Mark where platelets are.
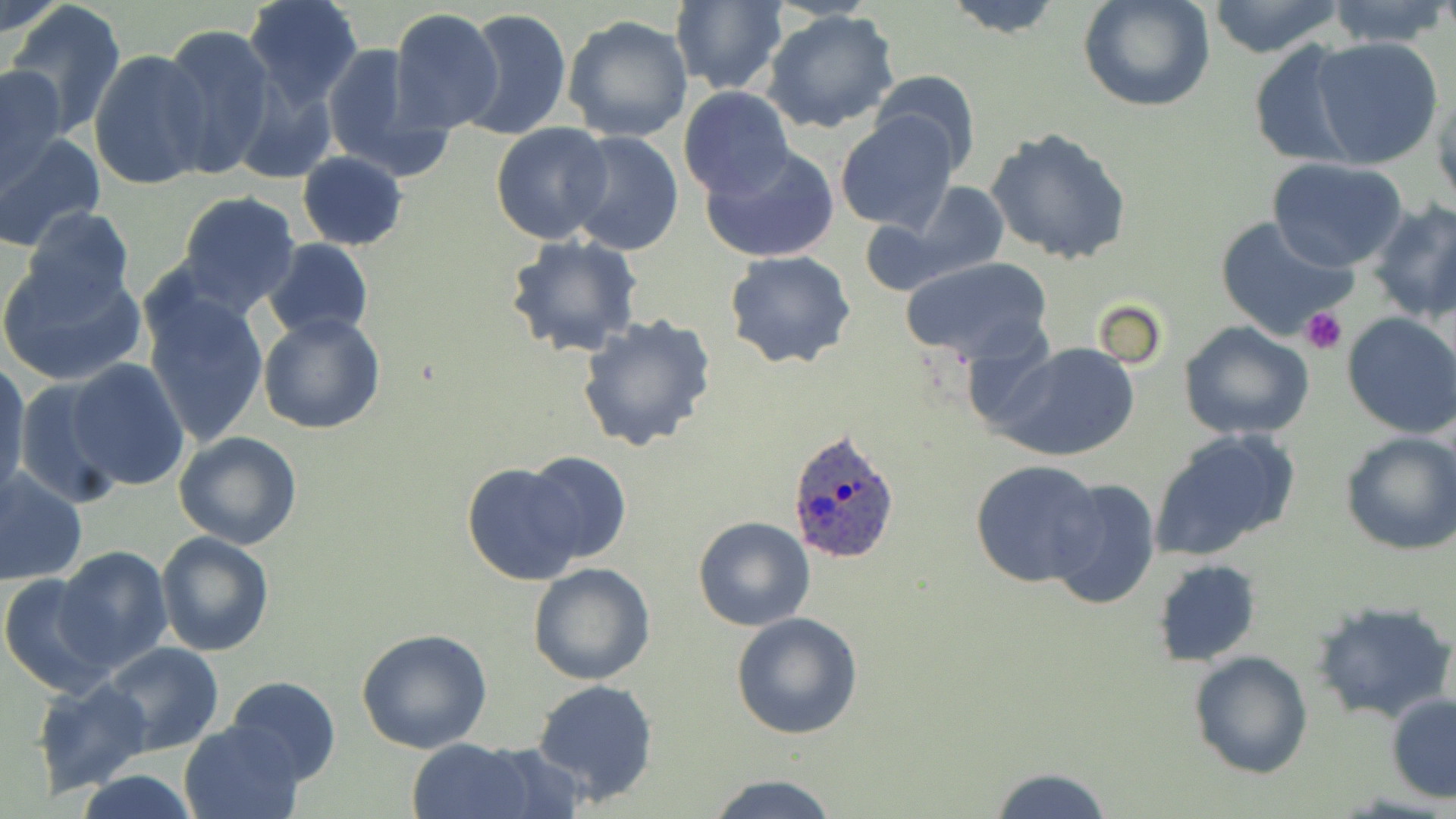

Approximate bounding boxes as [x1, y1, x2, y2] in pixels.
Platelets: [1299, 308, 1347, 355].

slide_level_diagnosis: Plasmodium ovale
preparation: thin blood film
uninfected_red_blood_cell_locations: 'approximate bounding boxes as [x1, y1, x2, y2] in pixels: [241, 0, 364, 106], [669, 0, 788, 96], [936, 0, 1068, 38], [1077, 0, 1216, 114], [1205, 0, 1346, 57], [1323, 0, 1455, 48], [1, 1, 68, 40], [5, 1, 128, 139], [389, 6, 503, 134], [457, 8, 573, 142], [763, 10, 901, 134], [562, 12, 693, 142], [158, 25, 280, 178], [1308, 37, 1444, 169], [320, 41, 450, 183], [1246, 43, 1365, 167], [87, 50, 214, 192], [2, 66, 70, 193], [869, 69, 981, 173], [228, 74, 338, 184], [677, 87, 796, 199], [835, 114, 958, 234], [491, 123, 616, 245], [983, 125, 1135, 267], [0, 128, 103, 250], [565, 131, 685, 256], [702, 144, 840, 264], [297, 151, 406, 250], [1267, 157, 1407, 272], [892, 181, 1012, 286], [177, 192, 303, 316], [1369, 200, 1456, 322], [20, 206, 136, 314], [1214, 216, 1358, 341], [504, 234, 644, 360], [263, 238, 375, 340], [724, 251, 858, 370], [900, 256, 1056, 368], [0, 258, 148, 387], [141, 288, 269, 448], [1343, 311, 1456, 438], [258, 312, 386, 434], [574, 312, 717, 453], [1178, 321, 1314, 440], [995, 343, 1143, 461], [67, 358, 191, 491], [1, 361, 30, 495], [10, 377, 125, 507], [1148, 428, 1301, 561], [174, 431, 303, 550], [1339, 431, 1456, 556], [521, 450, 632, 567], [971, 458, 1106, 588], [462, 462, 588, 585], [0, 467, 86, 587], [1045, 476, 1161, 611], [693, 516, 815, 631], [154, 530, 275, 657], [56, 546, 173, 672], [1152, 559, 1262, 667], [528, 562, 656, 685], [0, 573, 117, 698], [1309, 598, 1455, 725], [730, 611, 863, 740], [356, 629, 495, 754], [100, 640, 224, 757], [1188, 650, 1314, 778], [225, 674, 340, 785], [32, 677, 154, 797], [532, 678, 659, 803], [1386, 693, 1456, 802], [178, 718, 303, 819], [400, 740, 541, 819], [475, 741, 586, 817], [988, 766, 1112, 819], [75, 772, 197, 818], [707, 774, 841, 818]'
modality: optical microscopy
field_of_view: single
image_size: 1456×819 pixels
plasmodium_ovale_infected_red_blood_cell_locations: 'approximate bounding boxes as [x1, y1, x2, y2] in pixels: [787, 428, 903, 564]'
magnification: 1000x
stain: May-Grünwald-Giemsa